Identify the blood parasite species.
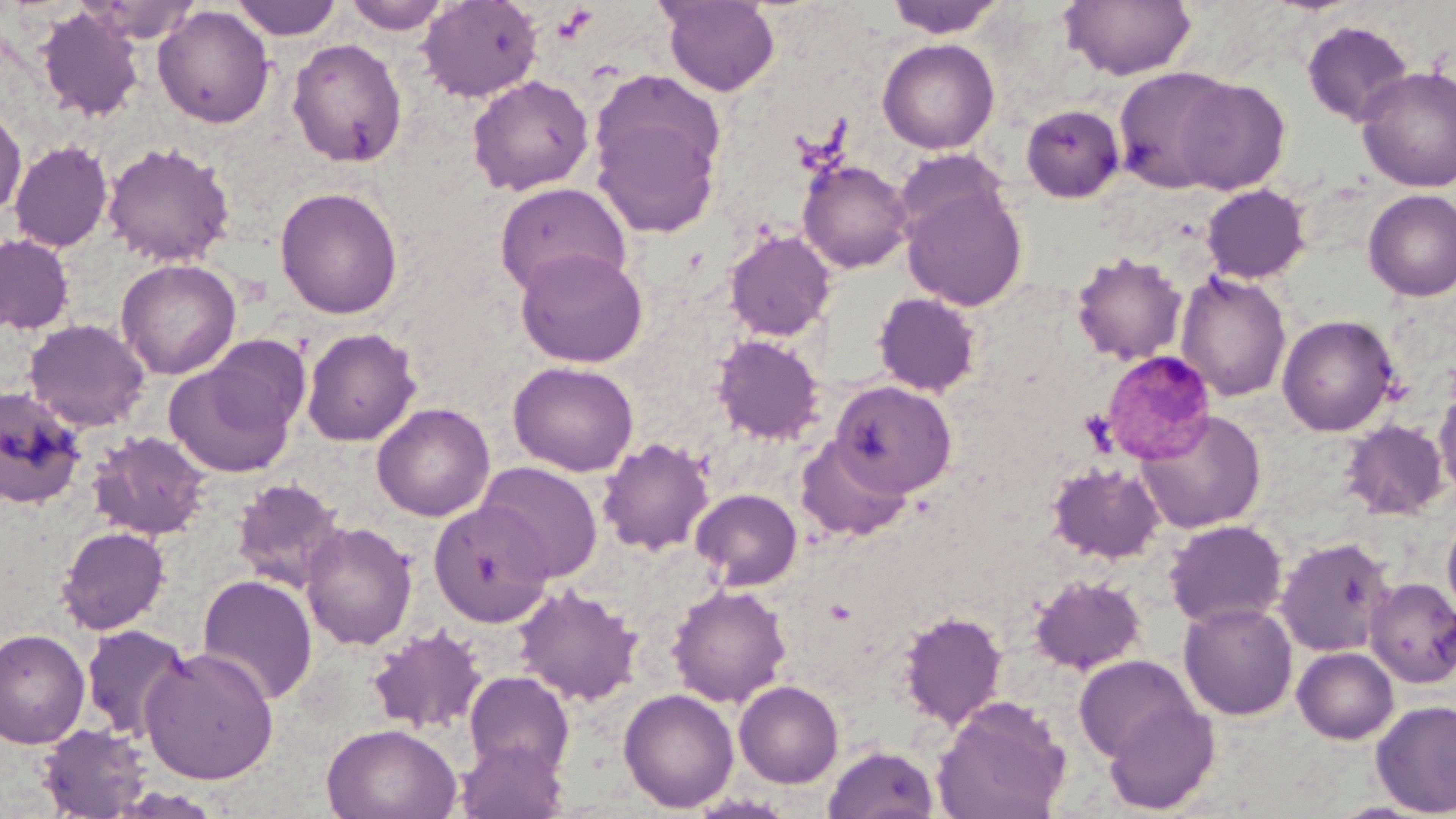
Plasmodium malariae.

Approximate bounding boxes as (x1, y1, x2, y2) in pixels. Platelet locations: (553, 5, 598, 43). Plasmodium malariae-infected red blood cell locations: (1101, 349, 1217, 464). Uninfected red blood cell locations: (230, 0, 343, 40), (344, 0, 451, 35), (417, 0, 543, 103), (658, 0, 780, 97), (884, 0, 1007, 38), (1059, 0, 1197, 80), (76, 1, 202, 43), (153, 5, 275, 129), (37, 7, 145, 122), (1301, 19, 1414, 128), (877, 38, 1000, 154), (288, 39, 408, 168), (1112, 66, 1240, 194), (1356, 66, 1456, 192), (467, 75, 594, 196), (1172, 76, 1291, 195), (591, 102, 723, 239), (1020, 104, 1124, 203), (0, 107, 27, 219), (8, 140, 114, 252), (102, 141, 235, 267), (894, 148, 1010, 245), (797, 158, 913, 274), (493, 182, 631, 297), (1200, 184, 1311, 284), (901, 185, 1028, 311), (274, 186, 404, 319), (1362, 189, 1456, 302), (723, 229, 836, 342), (0, 235, 75, 334), (514, 247, 650, 368), (1070, 251, 1188, 366), (116, 258, 241, 379), (1175, 271, 1292, 403), (872, 291, 983, 397), (1277, 314, 1400, 437), (23, 318, 151, 432), (301, 327, 421, 446), (202, 334, 312, 438), (711, 334, 825, 445), (164, 358, 298, 478), (507, 361, 639, 477), (830, 380, 956, 497), (1433, 385, 1456, 499), (0, 387, 86, 510), (371, 402, 495, 522), (1135, 409, 1267, 533), (1341, 419, 1449, 520), (88, 431, 212, 541), (795, 435, 912, 543), (597, 437, 714, 555), (475, 461, 603, 583), (1046, 461, 1165, 564), (231, 477, 346, 592), (690, 488, 803, 591), (428, 500, 554, 627), (1442, 506, 1456, 625), (1164, 519, 1287, 629), (300, 520, 418, 651), (56, 526, 171, 634), (1275, 536, 1396, 657), (197, 574, 318, 706), (1028, 574, 1146, 675), (1364, 578, 1456, 688), (513, 583, 643, 706), (666, 583, 793, 708), (1178, 601, 1297, 720), (898, 609, 1007, 729), (80, 624, 191, 741), (366, 624, 489, 736), (0, 628, 90, 749), (140, 646, 279, 784), (1292, 646, 1399, 744), (1072, 654, 1200, 763), (463, 670, 575, 777), (733, 680, 843, 787), (618, 687, 739, 813), (931, 695, 1071, 819), (1103, 697, 1221, 815), (1370, 700, 1456, 816), (37, 722, 152, 817), (322, 723, 462, 819), (456, 738, 568, 819), (823, 743, 940, 819). Image is 1456×819 pixels. Captured at 1000x magnification. Thin blood smear. One field of a larger specimen. May-Grünwald-Giemsa-stained preparation. Light microscopy.